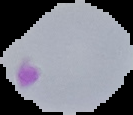 Malaria status: parasitized. Image is 133×115 pixels. From a thin blood film. Segmented cell region on a black background.